Assess this cell for malaria.
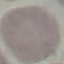
It is uninfected.

Acquired by smartphone through the microscope eyepiece. Thin blood film. Giemsa-stained preparation. Cell patch, automatically extracted from a larger field of view and resized to 64 × 64 pixels.